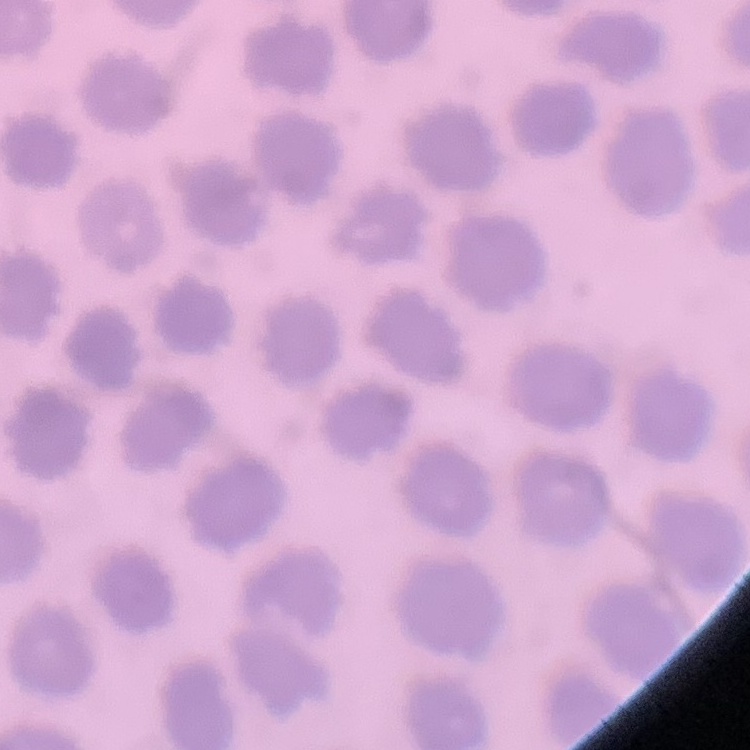

The erythrocytes exhibit no rouleaux formation. Stained with either Field's or Giemsa. One tile cut from a larger photomicrograph. Thin blood smear.